Assess this cell for malaria.
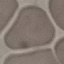

It is uninfected.

image_type: automatically extracted cell patch, resized to 64 × 64 pixels
capture: smartphone through the microscope eyepiece
preparation: thin blood smear
stain: Giemsa